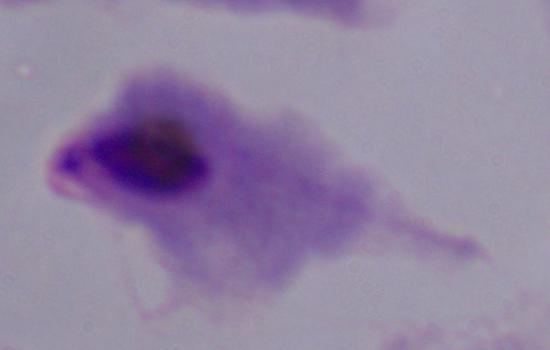

modality: micrograph
magnification: 1000x
identification: trichomonad